Locate every blood parasite and identify its species.
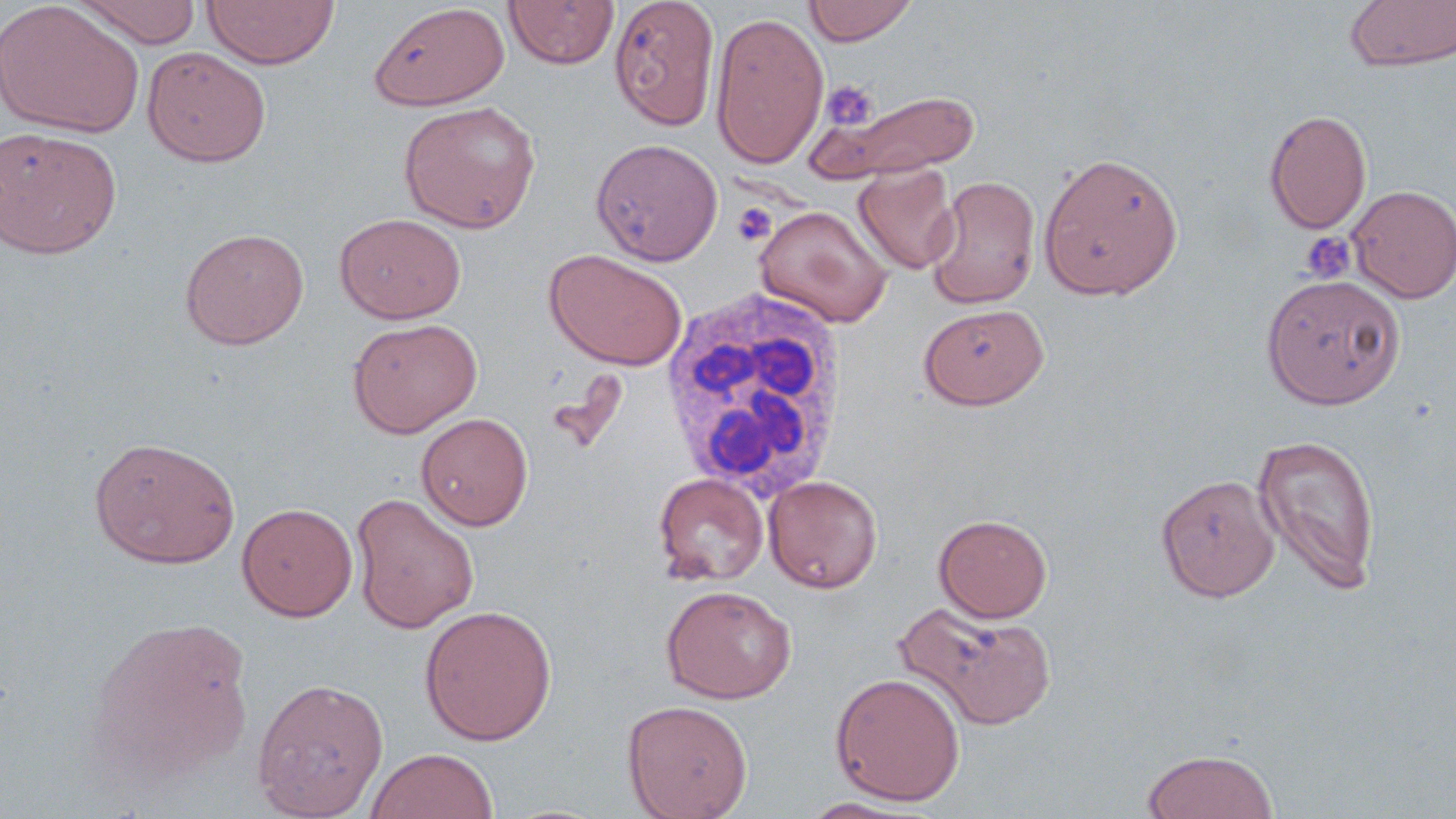

No blood parasites observed.

Summary:
  - Coordinate format: approximate bounding boxes as (x1,y1)-(x2,y2) corner pairs in pixels
  - Uninfected red blood cell locations: (73,0)-(202,48), (202,0)-(339,69), (608,0)-(720,131), (803,0)-(918,46), (1345,0)-(1456,72), (504,1)-(619,69), (0,2)-(145,139), (369,3)-(509,110), (710,10)-(829,169), (141,46)-(272,167), (818,88)-(982,181), (399,100)-(541,233), (1264,109)-(1372,234), (0,127)-(122,260), (591,138)-(723,265), (1038,151)-(1184,300), (853,165)-(960,275), (926,175)-(1042,308), (1347,185)-(1456,303), (754,205)-(892,327), (335,213)-(466,323), (179,227)-(310,349), (544,249)-(687,370), (1261,274)-(1404,409), (918,303)-(1050,409), (347,317)-(482,438), (416,412)-(533,531), (1253,433)-(1382,595), (88,436)-(241,569), (653,473)-(769,586), (763,474)-(883,593), (1156,474)-(1279,601), (350,491)-(480,634), (237,502)-(358,621), (934,514)-(1052,622), (661,584)-(797,703), (895,600)-(1058,731), (419,604)-(557,745), (87,615)-(256,782), (829,672)-(966,806), (251,677)-(389,819), (622,699)-(753,819), (364,747)-(499,819), (1141,748)-(1280,819), (798,797)-(930,818)
  - White blood cell locations: (661,282)-(850,504)
  - Platelet locations: (819,80)-(878,131), (732,203)-(777,246), (1299,230)-(1357,284)
  - Slide-level diagnosis: negative for blood parasites
  - Stain: May-Grünwald-Giemsa
  - Field of view: single
  - Modality: light microscopy
  - Magnification: 1000x
  - Preparation: thin blood smear
  - Image size: 1456×819 pixels